Locate and identify every blood parasite.
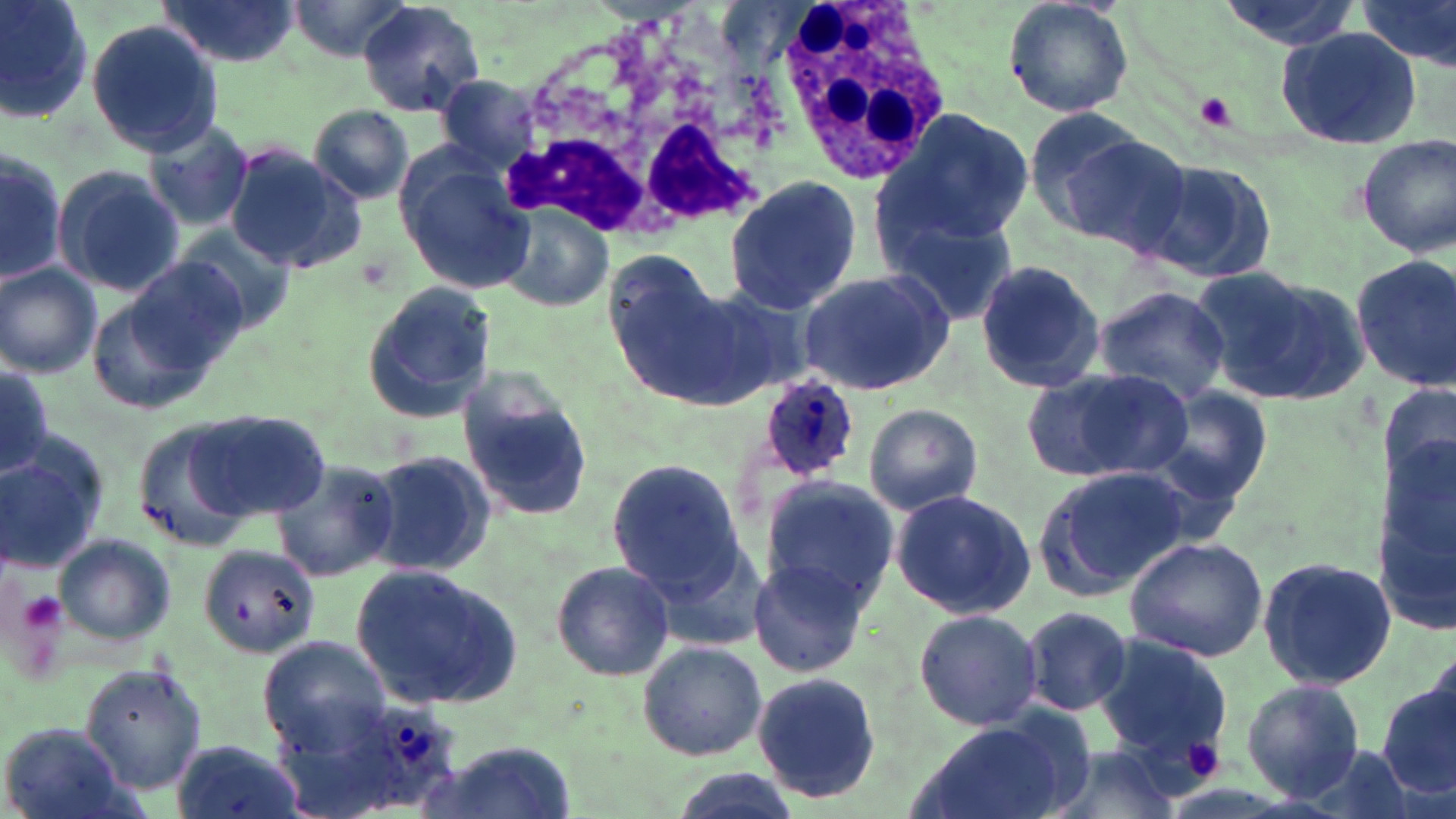

Approximate bounding boxes as (x1, y1, x2, y2) in pixels.
Plasmodium ovale-infected red blood cells: (755, 375, 859, 484), (345, 700, 461, 811).
No Plasmodium falciparum, Plasmodium malariae, Plasmodium vivax, Babesia divergens, or Trypanosoma brucei observed.

Uninfected red blood cell locations: (0, 0, 93, 125), (154, 0, 304, 69), (281, 0, 415, 61), (1001, 0, 1134, 120), (1212, 0, 1362, 51), (356, 1, 485, 118), (1357, 1, 1456, 70), (85, 18, 224, 156), (1277, 26, 1424, 150), (433, 74, 548, 175), (306, 105, 418, 206), (1018, 107, 1157, 232), (873, 109, 1033, 251), (141, 116, 256, 233), (1054, 126, 1196, 255), (1356, 135, 1456, 257), (224, 144, 366, 273), (0, 145, 67, 289), (394, 151, 535, 295), (1138, 156, 1280, 288), (50, 164, 187, 298), (723, 175, 866, 315), (498, 204, 615, 314), (886, 212, 1020, 326), (172, 225, 300, 336), (1349, 253, 1456, 395), (98, 259, 250, 403), (973, 259, 1106, 396), (0, 265, 102, 378), (1195, 266, 1368, 404), (797, 267, 957, 396), (360, 280, 495, 423), (611, 281, 745, 400), (1091, 285, 1232, 406), (0, 361, 55, 481), (1028, 367, 1185, 481), (460, 383, 595, 522), (1150, 387, 1272, 509), (863, 403, 982, 515), (187, 407, 331, 521), (130, 414, 270, 553), (1375, 434, 1455, 640), (0, 435, 111, 571), (361, 449, 498, 577), (605, 456, 745, 602), (271, 457, 400, 583), (1037, 464, 1195, 599), (760, 476, 899, 606), (890, 489, 1036, 618), (54, 533, 175, 644), (1124, 534, 1269, 662), (197, 543, 319, 656), (1257, 556, 1398, 689), (750, 558, 874, 678), (551, 559, 673, 680), (349, 564, 521, 710), (1021, 607, 1133, 717), (914, 608, 1043, 730), (1092, 635, 1233, 769), (259, 636, 387, 750), (636, 642, 767, 761), (77, 664, 208, 794), (751, 672, 882, 802), (1377, 676, 1456, 802), (1241, 678, 1365, 802), (272, 691, 400, 819), (909, 717, 1087, 819), (2, 724, 128, 818), (170, 734, 306, 819), (417, 741, 570, 819), (1039, 745, 1187, 819). Platelet locations: (1197, 92, 1236, 131), (15, 589, 67, 639), (1179, 736, 1229, 783). White blood cell locations: (776, 1, 949, 186), (495, 5, 784, 252). Slide-level diagnosis: Plasmodium ovale. Light microscopy. May-Grünwald-Giemsa-stained preparation. 1000x magnification. One field of a larger specimen. Image is 1456×819 pixels. Thin blood film.